Give the position of every leukocyte visible.
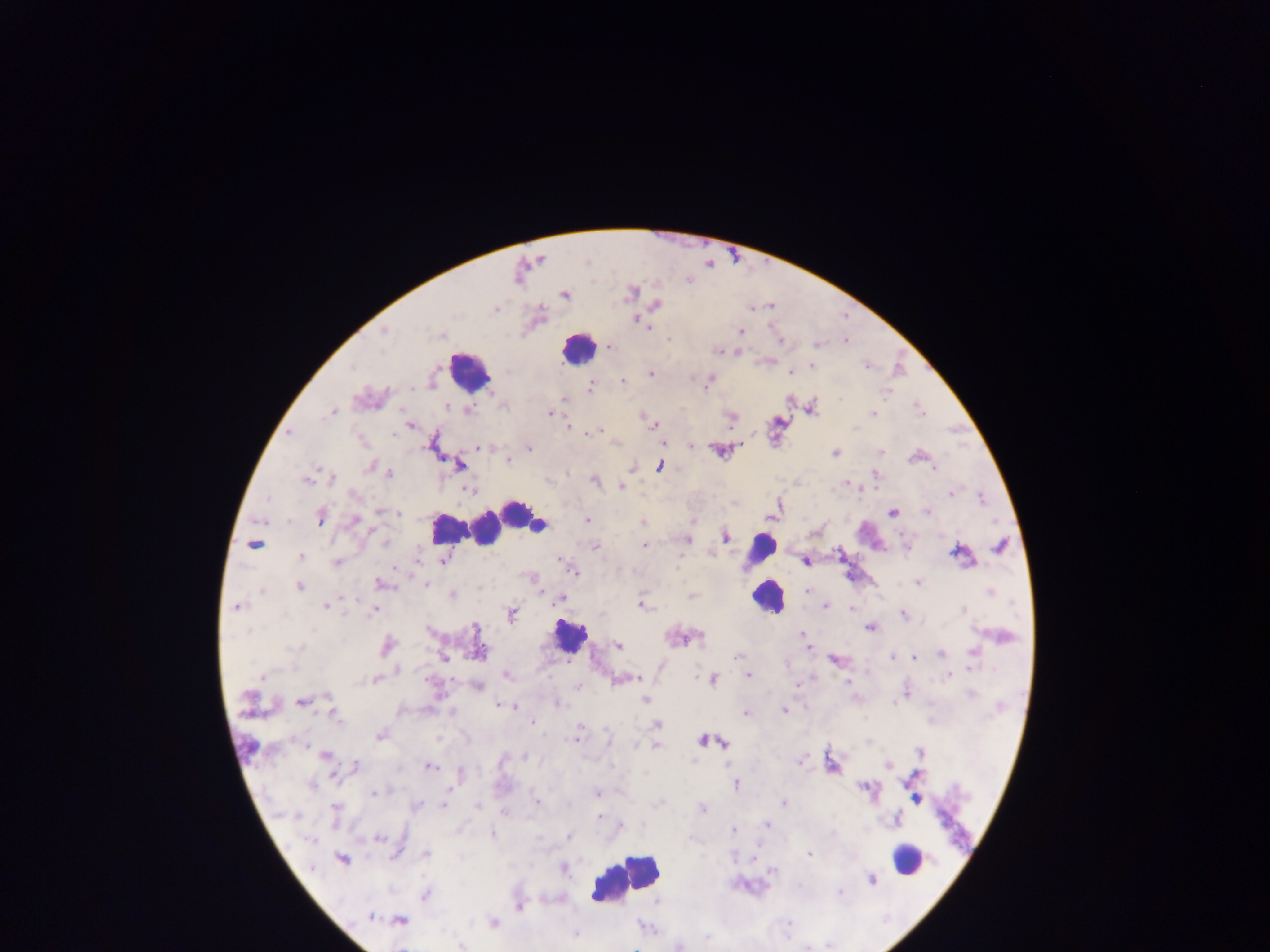

Approximate centers as x y in pixels.
Leukocytes: 577 348; 468 370; 519 514; 487 527; 447 528; 538 528; 466 529; 869 533; 761 549; 766 598; 569 637; 906 857; 626 878.

Malaria parasite locations: 630 293; 564 295; 657 304; 638 321; 647 327; 383 331; 741 332; 670 339; 781 340; 816 344; 611 347; 719 350; 867 365; 351 366; 812 366; 790 371; 651 373; 623 381; 709 381; 590 388; 887 391; 565 400; 446 406; 920 409; 469 411; 330 412; 550 413; 873 414; 643 417; 730 418; 651 423; 410 426; 568 426; 596 432; 289 433; 362 441; 662 441; 691 445; 480 447; 529 448; 880 452; 836 453; 507 460; 459 465; 370 466; 659 467; 934 468; 389 474; 332 478; 306 480; 594 481; 846 483; 622 486; 469 489; 951 493; 354 494; 267 499; 981 499; 381 511; 398 513; 892 513; 927 513; 772 515; 320 518; 355 519; 587 520; 643 522; 726 537; 686 540; 385 542; 253 544; 645 545; 594 547; 1000 547; 907 548; 956 552; 300 556; 443 560; 805 561; 337 563; 573 572; 532 579; 918 583; 382 584; 425 584; 299 587; 808 590; 262 592; 990 592; 452 595; 691 595; 559 599; 642 605; 826 605; 326 606; 237 607; 853 609; 373 610; 964 610; 511 614; 904 615; 475 628; 870 628; 802 634; 1004 637; 698 638; 387 646; 618 646; 807 646; 295 648; 479 648; 941 652; 973 652; 738 655; 892 656; 444 658; 914 658; 834 659; 749 675; 261 676; 507 676; 949 676; 625 679; 374 680; 713 680; 848 682; 798 685; 478 687; 577 687; 907 693; 972 694; 328 697; 247 698; 645 699; 302 701; 894 703; 558 705; 504 706; 785 711; 745 713; 336 716; 533 722; 656 724; 379 736; 575 738; 702 740; 725 743; 655 746; 920 753; 325 755; 526 757; 693 761; 800 761; 887 765; 356 766; 429 767; 461 774; 735 785; 311 786; 374 793; 596 793; 917 799; 537 801; 659 804; 783 804; 416 805; 443 805; 478 806; 702 809; 335 811; 505 812; 296 816; 598 816; 621 825; 767 825; 734 830; 493 835; 569 837; 378 840; 310 841; 426 854; 809 855; 341 860; 564 869; 775 870; 872 879; 840 893; 426 895; 520 906; 371 917; 400 921; 493 923; 575 935; 707 937; 680 947. Single field of view. Collected in Ghana. Thick blood film. Photographed through a microscope with a mobile-phone camera. Image is 1270×952 pixels.